Assess for Plasmodium parasites.
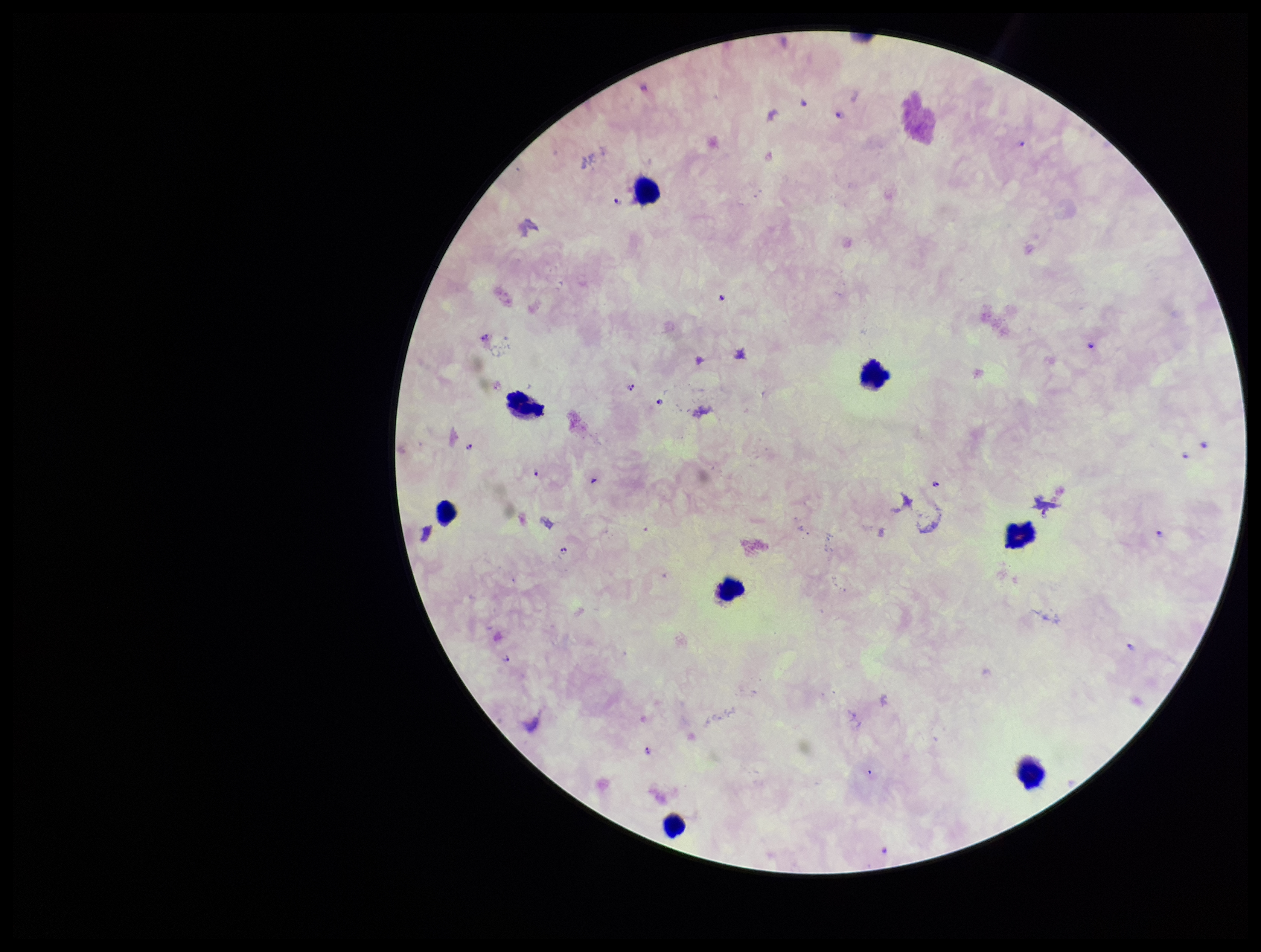

Detected.

Summary:
  - Field of view: one from this slide
  - Capture: smartphone photograph through the microscope eyepiece
  - Preparation: thick smear
  - Image size: 1261×952 pixels
  - Parasite count: 18
  - Leukocyte count: 8
  - Species reported for this patient: Plasmodium falciparum
  - Patient malaria status: positive
  - Stain: Giemsa